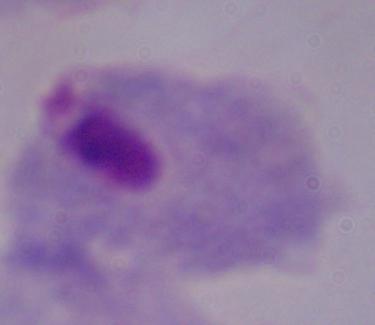
Summary:
  - Magnification: 1000x
  - Modality: micrograph
  - Identification: trichomonad